State which parasite is depicted.
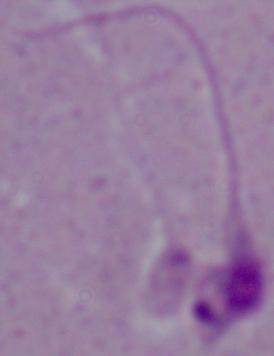

This is Leishmania.

modality: photomicrograph
magnification: 1000x